Locate and identify every blood parasite.
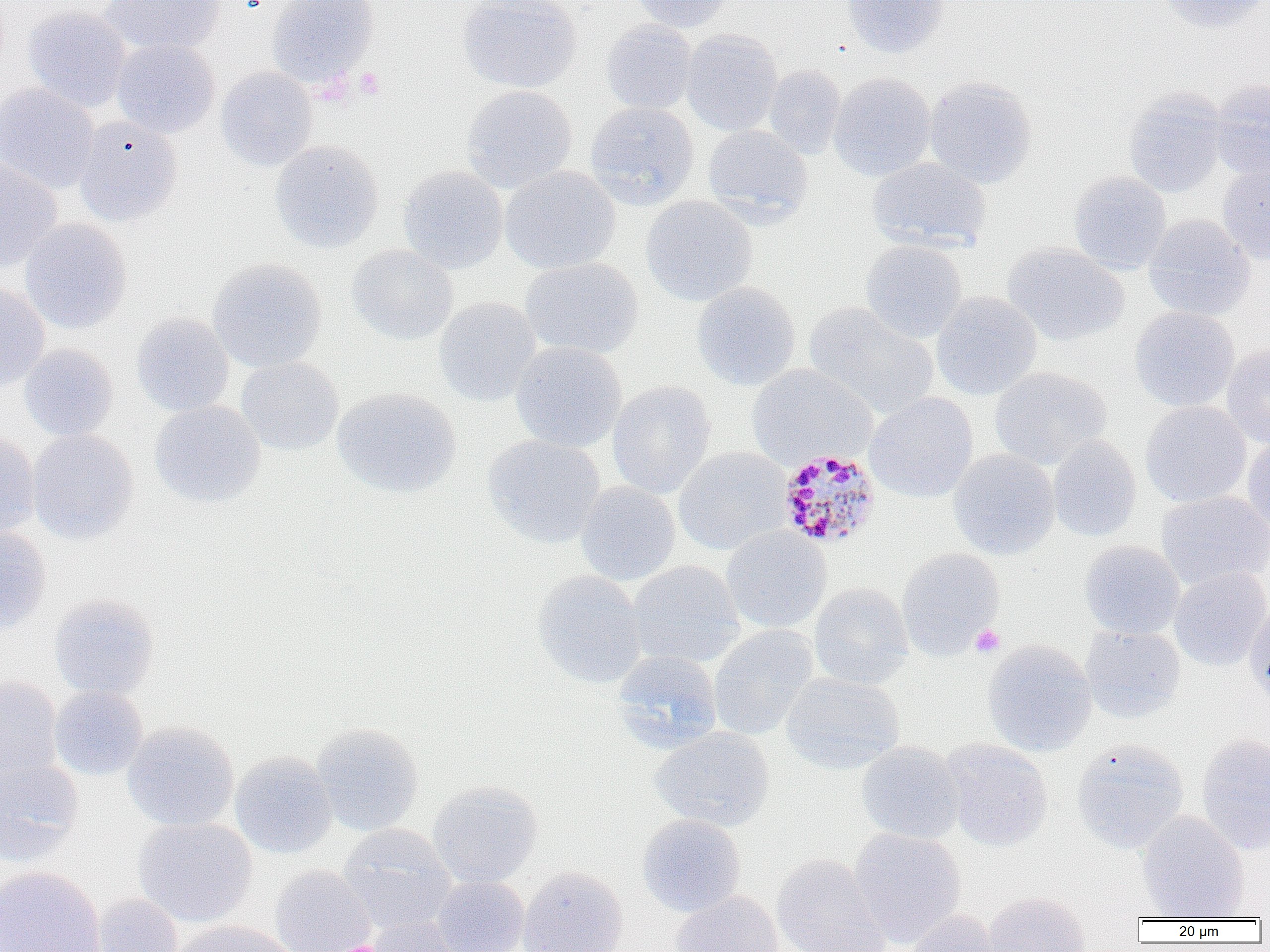
Approximate bounding boxes as (x1,y1)-(x2,y2) corner pairs in pixels.
Plasmodium malariae-infected red blood cells: (776,448)-(881,550).
No Plasmodium falciparum, Plasmodium ovale, Plasmodium vivax, Babesia divergens, or Trypanosoma brucei observed.

Platelet locations: (355,66)-(385,99), (970,624)-(1005,657). Uninfected red blood cell locations: (99,0)-(225,55), (267,0)-(380,86), (457,0)-(582,93), (630,0)-(734,32), (841,0)-(950,59), (1155,0)-(1270,33), (22,5)-(132,112), (600,19)-(698,114), (681,29)-(783,136), (111,39)-(220,138), (763,66)-(845,159), (216,67)-(318,172), (829,72)-(936,181), (924,76)-(1037,188), (1210,78)-(1270,180), (0,83)-(99,194), (462,85)-(578,192), (1123,89)-(1228,197), (585,102)-(699,209), (73,115)-(183,227), (702,125)-(813,224), (269,140)-(384,253), (0,156)-(63,273), (867,157)-(991,252), (1217,159)-(1270,266), (398,166)-(508,274), (499,166)-(620,275), (1069,171)-(1171,274), (640,195)-(758,306), (1143,215)-(1256,321), (19,218)-(132,334), (860,240)-(967,342), (1003,243)-(1129,346), (346,244)-(458,346), (207,257)-(326,372), (520,257)-(643,360), (692,281)-(802,391), (0,282)-(49,392), (931,291)-(1042,400), (433,296)-(541,406), (804,302)-(939,419), (1129,306)-(1239,412), (131,312)-(235,416), (511,342)-(627,453), (1221,342)-(1270,448), (19,344)-(119,441), (236,357)-(344,456), (747,364)-(876,470), (990,366)-(1111,469), (607,380)-(716,499), (332,387)-(461,498), (864,392)-(977,503), (149,400)-(266,508), (1140,401)-(1251,507), (27,429)-(138,544), (0,430)-(40,539), (482,435)-(605,549), (1047,435)-(1141,542), (1243,435)-(1270,534), (673,447)-(793,555), (948,449)-(1060,560), (576,481)-(680,585), (1156,491)-(1270,589), (721,526)-(831,633), (0,527)-(51,635), (1079,541)-(1185,639), (896,547)-(1004,658), (627,560)-(745,669), (1169,567)-(1270,670), (532,571)-(647,688), (809,582)-(914,689), (49,594)-(160,701), (1244,605)-(1270,708), (708,625)-(819,740), (1080,625)-(1186,723), (982,640)-(1097,757), (611,651)-(723,753), (781,672)-(905,774), (0,675)-(62,780), (49,686)-(148,780), (122,721)-(239,832), (311,723)-(424,836), (648,726)-(775,832), (1196,733)-(1270,855), (940,739)-(1053,852), (1072,739)-(1189,852), (856,741)-(964,844), (230,751)-(337,859), (0,758)-(83,865), (427,780)-(543,888), (1137,811)-(1249,920), (637,814)-(746,917), (132,816)-(258,928), (338,823)-(456,934), (848,827)-(967,948), (771,853)-(891,951), (269,864)-(376,952), (518,865)-(629,952), (0,866)-(105,952), (431,875)-(529,952), (669,891)-(784,952), (984,891)-(1092,952), (90,894)-(183,952), (903,909)-(1005,952), (365,917)-(468,952), (170,920)-(296,952). Slide-level diagnosis: Plasmodium malariae. Light microscopy. 1000x magnification. Thin blood smear. Image is 1270×952 pixels. One field of a larger specimen.